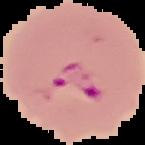

Result: malaria parasites detected. Cell region segmented out of the field of view; the surrounding area is masked to black. From a thin blood smear. Image is 145×145 pixels.